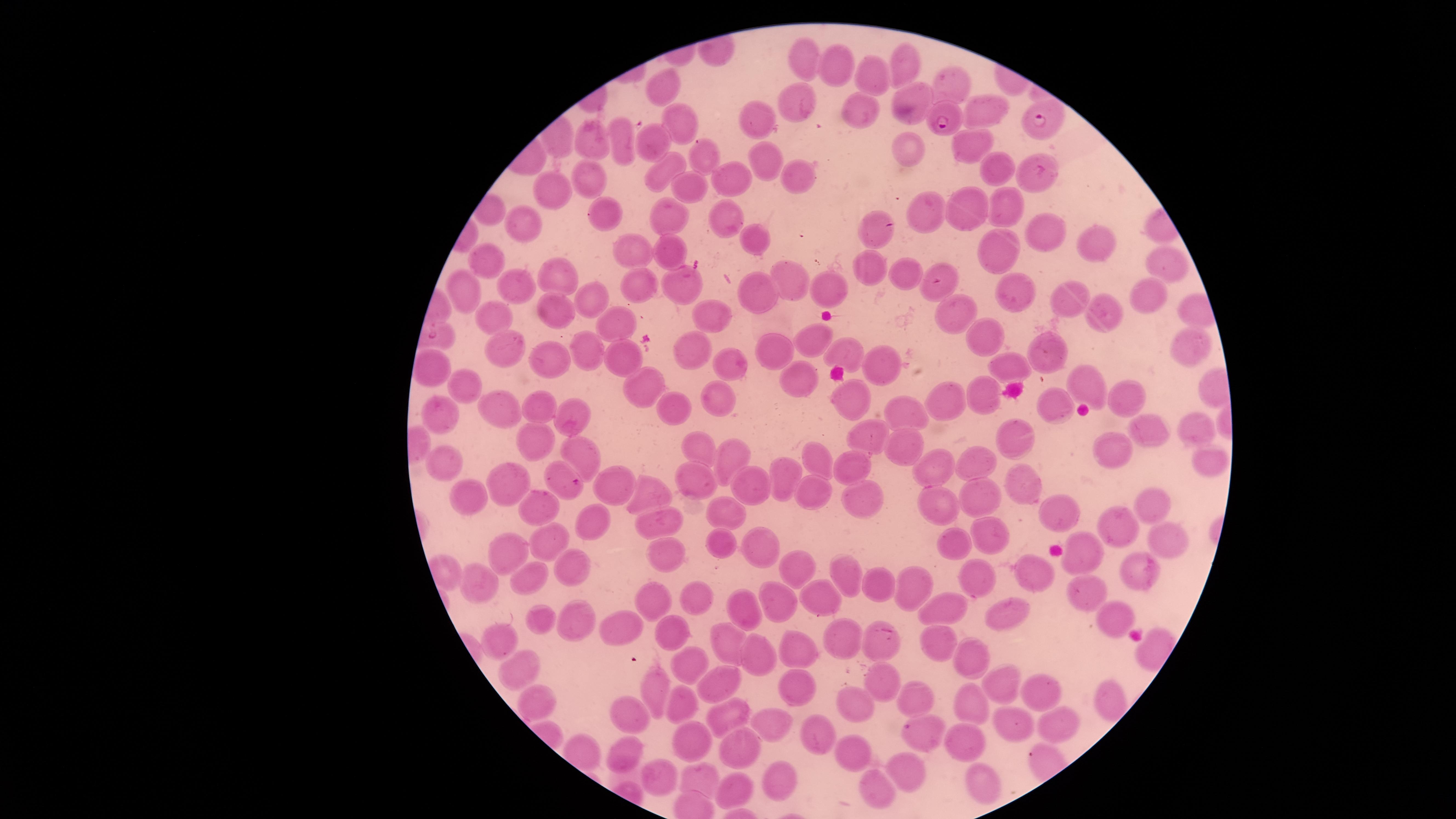 Approximate marker points as {x, y} in pixels. Uninfected red blood cells: {807, 61}, {901, 61}, {839, 64}, {876, 72}, {950, 82}, {665, 86}, {917, 95}, {795, 100}, {984, 111}, {859, 112}, {758, 119}, {680, 120}, {621, 142}, {653, 142}, {596, 144}, {903, 144}, {968, 146}, {767, 156}, {699, 158}, {992, 168}, {663, 169}, {1041, 173}, {735, 175}, {793, 177}, {595, 181}, {691, 185}, {554, 190}, {1004, 206}, {967, 209}, {929, 211}, {600, 212}, {723, 213}, {668, 215}, {526, 225}, {1040, 228}, {870, 229}, {762, 240}, {636, 248}, {673, 248}, {1100, 248}, {998, 256}, {490, 263}, {1163, 263}, {868, 270}, {784, 273}, {905, 274}, {559, 275}, {675, 281}, {517, 282}, {643, 287}, {940, 289}, {829, 290}, {467, 291}, {760, 292}, {1151, 293}, {1012, 295}, {589, 297}, {1066, 297}, {547, 308}, {1102, 311}, {960, 315}, {710, 316}, {490, 317}, {623, 321}, {985, 333}, {810, 335}, {774, 341}, {505, 344}, {1187, 346}, {586, 351}, {697, 352}, {1054, 352}, {620, 353}, {845, 353}, {548, 357}, {730, 360}, {1007, 365}, {884, 367}, {802, 378}, {1086, 383}, {641, 385}, {469, 387}, {985, 396}, {723, 397}, {849, 397}, {1124, 398}, {947, 400}, {540, 404}, {668, 404}, {1058, 405}, {441, 409}, {500, 410}, {569, 414}, {908, 418}, {1142, 428}, {1192, 432}, {871, 435}, {1020, 436}, {540, 442}, {1112, 445}, {906, 446}, {704, 449}, {583, 452}, {734, 455}, {819, 462}, {1208, 462}, {443, 464}, {984, 466}, {847, 467}, {941, 469}, {555, 473}, {779, 476}, {693, 477}, {513, 484}, {755, 485}, {1023, 485}, {617, 487}, {648, 492}, {464, 494}, {813, 494}, {855, 496}, {967, 497}, {539, 501}, {937, 506}, {1150, 506}, {727, 511}, {591, 516}, {1061, 517}, {655, 520}, {1120, 531}, {545, 536}, {995, 538}, {1166, 543}, {723, 544}, {956, 544}, {764, 545}, {512, 551}, {668, 554}, {1088, 554}, {567, 567}, {798, 567}, {1131, 571}, {1027, 572}, {534, 574}, {848, 574}, {984, 577}, {483, 580}, {911, 585}, {879, 588}, {1088, 593}, {694, 596}, {659, 597}, {780, 602}, {742, 603}, {819, 603}, {944, 610}, {1008, 614}, {1111, 614}, {539, 619}, {574, 620}, {620, 626}, {672, 630}, {503, 634}, {843, 639}, {874, 641}, {728, 643}, {803, 646}, {943, 646}, {763, 658}, {969, 658}, {687, 660}, {515, 666}, {1005, 680}, {880, 681}, {724, 682}, {794, 686}, {1035, 688}, {656, 692}, {913, 698}, {1109, 698}, {536, 703}, {686, 703}, {866, 705}, {972, 706}, {732, 710}, {629, 712}, {1051, 723}, {777, 724}, {1007, 724}, {813, 733}, {965, 736}, {926, 737}, {687, 742}, {852, 750}, {621, 751}, {739, 752}, {904, 768}, {662, 775}, {778, 776}, {700, 778}, {982, 780}, {733, 789}, {877, 789}. Parasitized red blood cells: {950, 115}, {1048, 122}. Thin blood film. Photographed with a smartphone camera through the microscope eyepiece. Giemsa stain. The visible region is circular. Image is 1456×819 pixels. One field of view of the specimen. Presence: malaria parasites seen. Species: Plasmodium falciparum.